Name the blood parasite species.
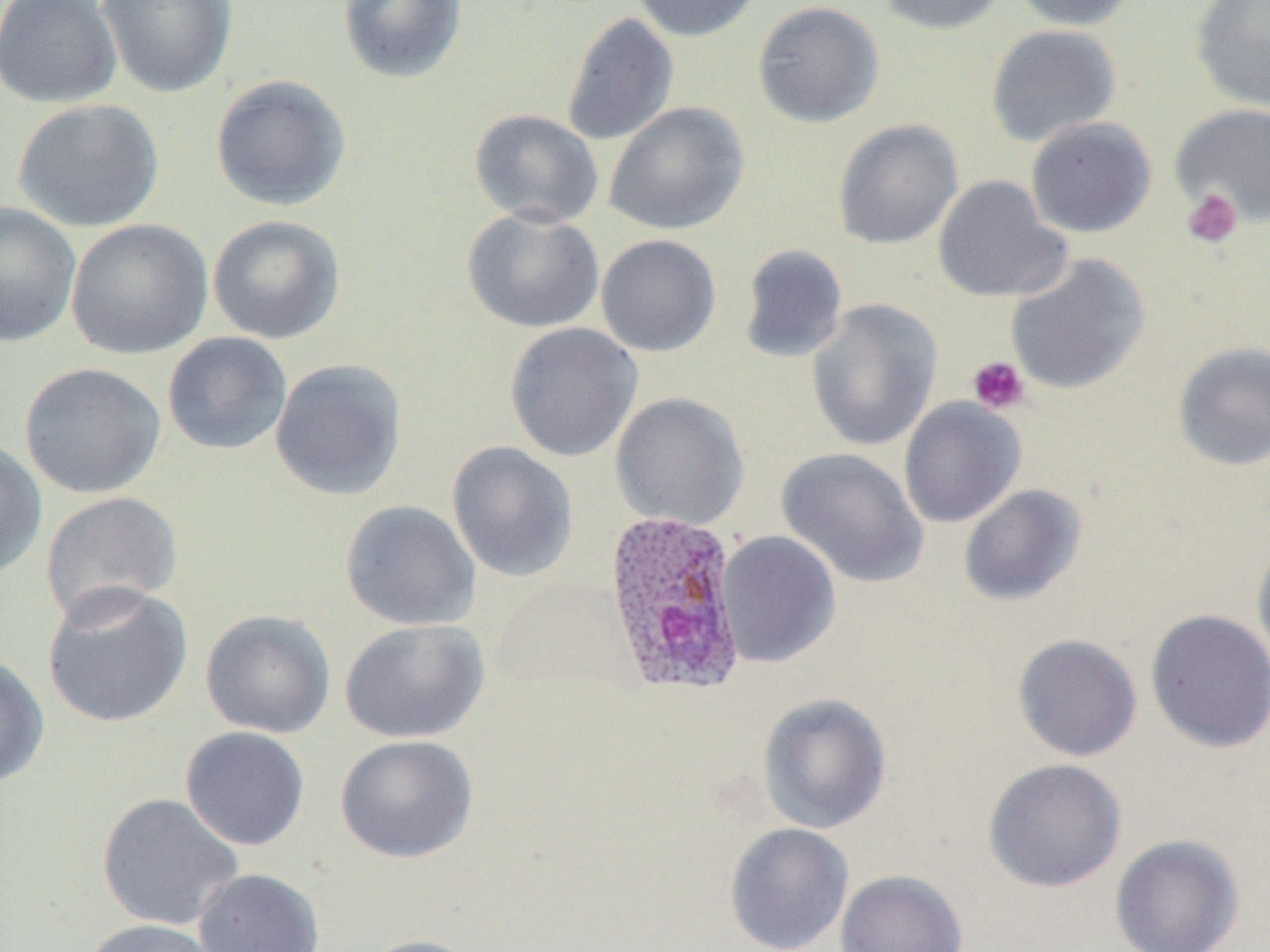
Plasmodium ovale.

Summary:
  - Coordinate format: approximate bounding boxes as (x1, y1, x2, y2) in pixels
  - Plasmodium ovale-infected red blood cell locations: (603, 509, 748, 695)
  - Platelet locations: (1181, 188, 1243, 250), (968, 356, 1030, 414)
  - Uninfected red blood cell locations: (0, 0, 122, 108), (96, 0, 238, 99), (337, 0, 468, 84), (629, 0, 763, 42), (874, 0, 1010, 35), (1009, 0, 1140, 31), (752, 1, 885, 128), (1190, 1, 1270, 112), (561, 12, 679, 146), (985, 24, 1121, 148), (210, 74, 352, 212), (12, 98, 164, 232), (604, 101, 750, 236), (1170, 102, 1270, 229), (469, 109, 603, 228), (1025, 117, 1157, 238), (833, 119, 963, 250), (932, 175, 1072, 303), (0, 201, 81, 347), (461, 208, 605, 334), (207, 214, 346, 345), (65, 218, 213, 360), (596, 234, 721, 357), (738, 244, 849, 364), (1005, 254, 1150, 395), (805, 299, 943, 451), (503, 322, 643, 462), (162, 332, 292, 456), (1171, 341, 1270, 472), (269, 358, 408, 501), (18, 362, 166, 499), (610, 392, 750, 531), (898, 397, 1026, 527), (0, 439, 47, 581), (446, 441, 578, 582), (777, 447, 928, 588), (958, 483, 1086, 606), (39, 491, 183, 624), (339, 499, 481, 631), (716, 530, 841, 667), (1252, 538, 1270, 676), (42, 582, 193, 728), (1145, 609, 1270, 753), (200, 610, 336, 739), (338, 618, 490, 744), (1011, 633, 1142, 762), (0, 654, 49, 790), (758, 692, 892, 834), (180, 726, 310, 851), (335, 734, 478, 863), (983, 758, 1127, 892), (96, 792, 243, 932), (724, 822, 854, 952), (1110, 833, 1244, 952), (192, 868, 325, 952), (835, 869, 968, 952), (79, 919, 226, 952), (360, 934, 485, 952)
  - Modality: optical microscopy
  - Field of view: one of a larger specimen
  - Stain: May-Grünwald-Giemsa
  - Magnification: 1000x
  - Preparation: thin blood smear
  - Image size: 1270×952 pixels